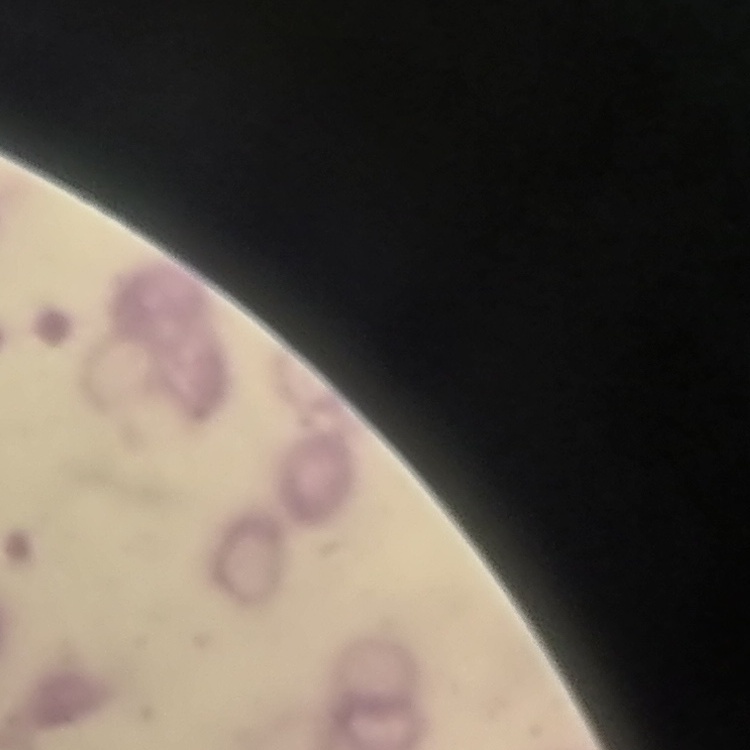

The red blood cells show rouleaux formation. Thin blood film. Stained with either Field's or Giemsa. One tile cut from a larger photomicrograph.